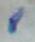

Toxoplasma gondii is seen. 1000x magnification. Micrograph.